Report the malaria status of this cell.
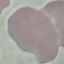

It is uninfected.

Photographed with a smartphone camera at the microscope eyepiece. Giemsa stain. Cell patch, automatically extracted from a larger field of view and resized to 64 × 64 pixels. Thin blood film.